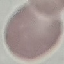

Summary:
  - Malaria status: uninfected
  - Image type: automatically extracted cell patch, resized to 64 × 64 pixels
  - Preparation: thin smear
  - Capture: smartphone camera at the microscope eyepiece
  - Stain: Giemsa